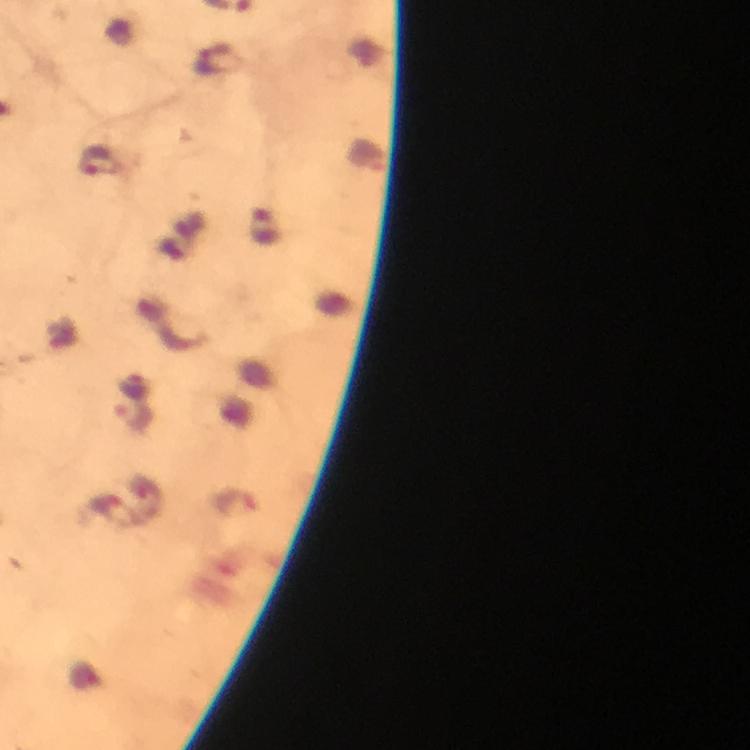

Approximate object centers, in pixels from the top-left corner. Plasmodium parasite locations: (x=218, y=60), (x=99, y=162), (x=265, y=228), (x=133, y=418), (x=234, y=505). Smartphone photograph taken through a microscope. Giemsa-stained preparation. Image is 750×750 pixels. A crop from one field of view. Thick smear. Immersion oil applied. 100x magnification. From a malaria diagnostic workup.